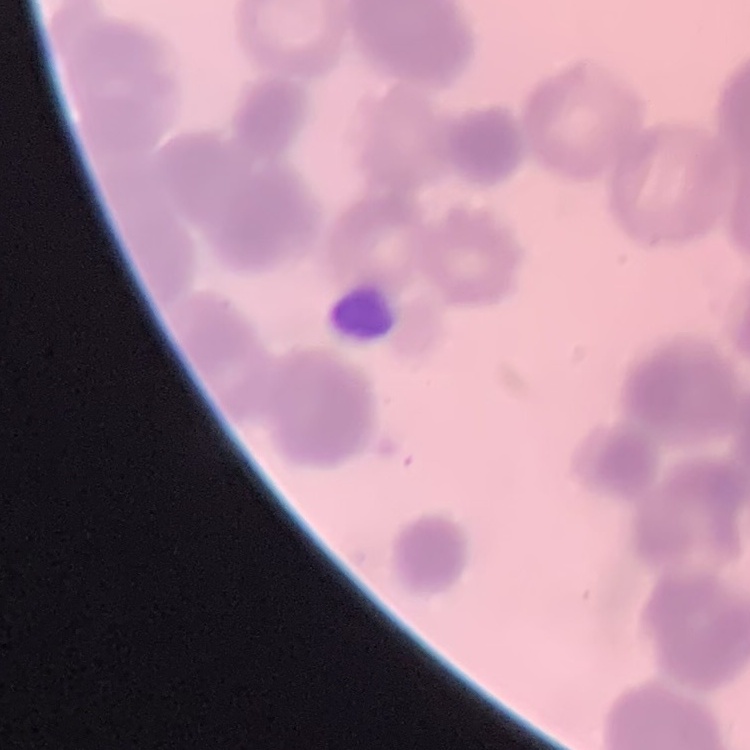
Summary:
  - Erythrocyte morphology: rouleaux formation
  - Image type: square crop of a larger photomicrograph
  - Stain: Field's or Giemsa
  - Preparation: thin blood film